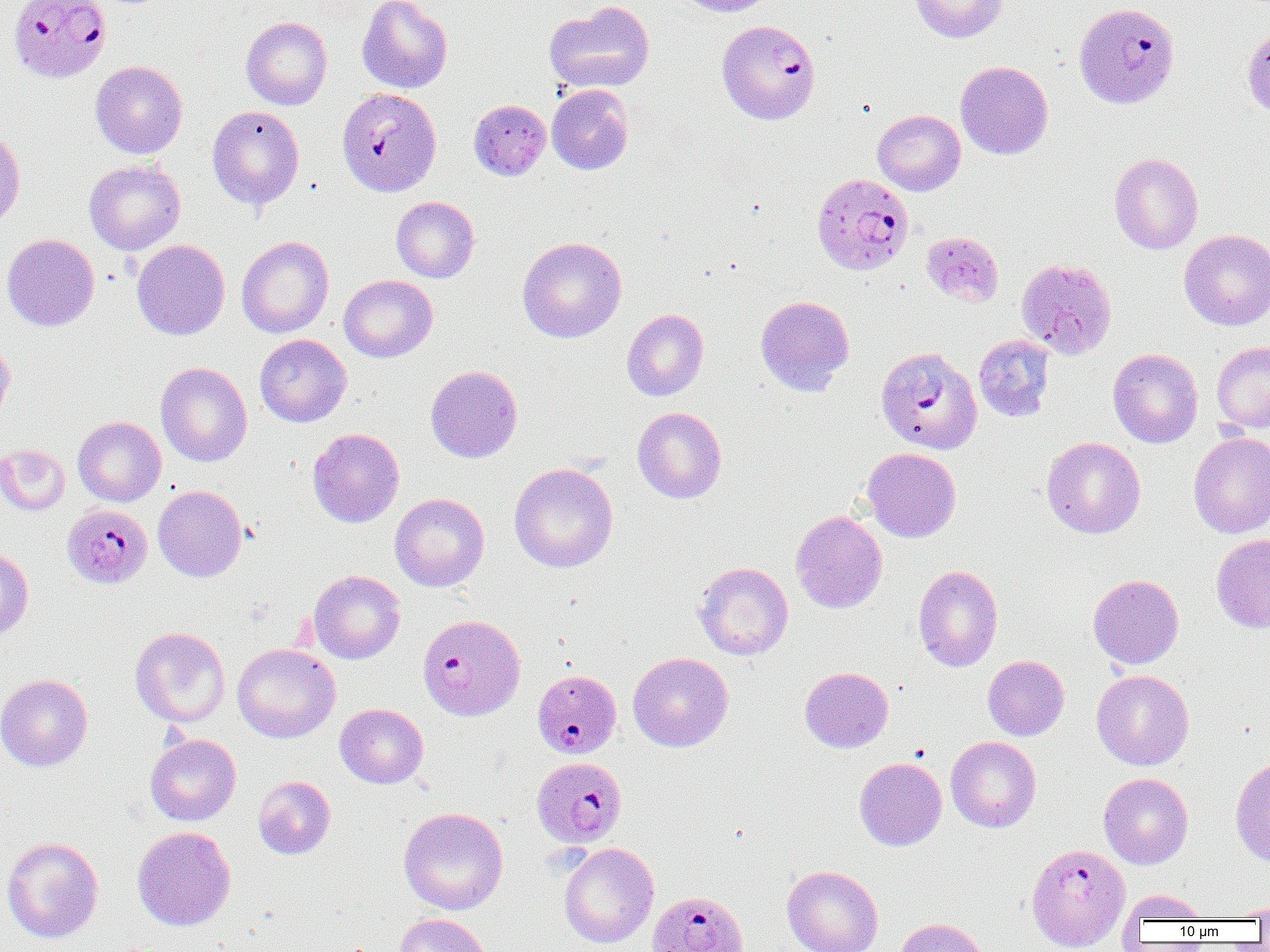
Approximate bounding boxes as [x1, y1, x2, y2] in pixels. Uninfected red blood cell locations: [356, 0, 453, 94], [671, 0, 779, 17], [910, 0, 1008, 43], [544, 1, 655, 93], [241, 16, 332, 110], [1242, 24, 1270, 120], [90, 60, 188, 158], [955, 61, 1053, 159], [547, 84, 634, 175], [469, 99, 551, 180], [207, 105, 304, 210], [873, 109, 965, 195], [0, 129, 25, 229], [1109, 153, 1203, 254], [84, 158, 185, 255], [391, 196, 479, 282], [1179, 229, 1270, 331], [920, 231, 1004, 307], [2, 234, 99, 331], [236, 235, 334, 338], [517, 236, 627, 343], [132, 239, 230, 340], [339, 275, 438, 362], [755, 295, 855, 395], [621, 309, 708, 401], [254, 334, 352, 427], [973, 335, 1055, 422], [0, 338, 14, 427], [1211, 340, 1270, 434], [1108, 348, 1203, 448], [155, 362, 253, 467], [425, 365, 523, 463], [633, 406, 726, 504], [73, 416, 166, 506], [308, 428, 404, 527], [1189, 432, 1270, 538], [1041, 437, 1145, 539], [0, 444, 70, 516], [861, 447, 961, 542], [509, 462, 618, 573], [153, 485, 247, 582], [390, 493, 489, 592], [790, 510, 888, 613], [1210, 533, 1270, 633], [0, 547, 33, 639], [693, 561, 793, 660], [913, 565, 1003, 672], [308, 570, 405, 664], [1088, 574, 1184, 669], [130, 626, 230, 727], [232, 643, 340, 743], [628, 652, 733, 752], [983, 655, 1069, 741], [800, 666, 893, 752], [1091, 669, 1194, 770], [0, 674, 93, 771], [335, 703, 428, 789], [145, 733, 241, 826], [945, 736, 1041, 832], [854, 757, 947, 851], [1230, 757, 1270, 866], [1099, 772, 1193, 869], [253, 776, 336, 859], [398, 806, 508, 915], [132, 826, 235, 931], [2, 836, 104, 943], [559, 843, 659, 948], [782, 865, 883, 952], [1120, 888, 1209, 925], [1233, 902, 1270, 920], [392, 913, 494, 952], [894, 917, 991, 952]. Plasmodium falciparum-infected red blood cell locations: [8, 0, 111, 84], [1077, 3, 1182, 109], [717, 19, 821, 125], [337, 88, 442, 196], [811, 172, 914, 276], [1016, 257, 1117, 360], [878, 347, 985, 455], [63, 504, 152, 588], [418, 614, 525, 721], [533, 669, 621, 759], [532, 757, 627, 848], [1027, 844, 1130, 950], [647, 890, 749, 952]. Slide-level diagnosis: Plasmodium falciparum. Image is 1270×952 pixels. Optical microscopy. 1000x magnification. Single field of view. Thin blood film.